Identify the parasite.
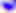

Toxoplasma gondii.

magnification = 400x
modality = micrograph